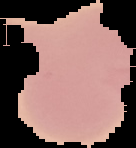
Summary:
  - Malaria status: uninfected
  - Image type: segmented cell region on a black background
  - Image size: 136×148 pixels
  - Preparation: thin blood smear